State which parasite is depicted.
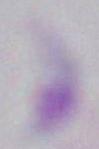
Toxoplasma gondii.

Photomicrograph. Captured at 1000x magnification.